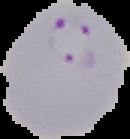

{
  "preparation": "thin blood film",
  "image_type": "segmented cell region on a black background",
  "image_size": "130×139 pixels",
  "result": "Plasmodium parasites identified"
}